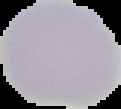 From a thin blood film. Image is 121×109 pixels. Result: no Plasmodium parasites seen. The area outside the segmented cell region is set to black.